Mark where leukocytes are.
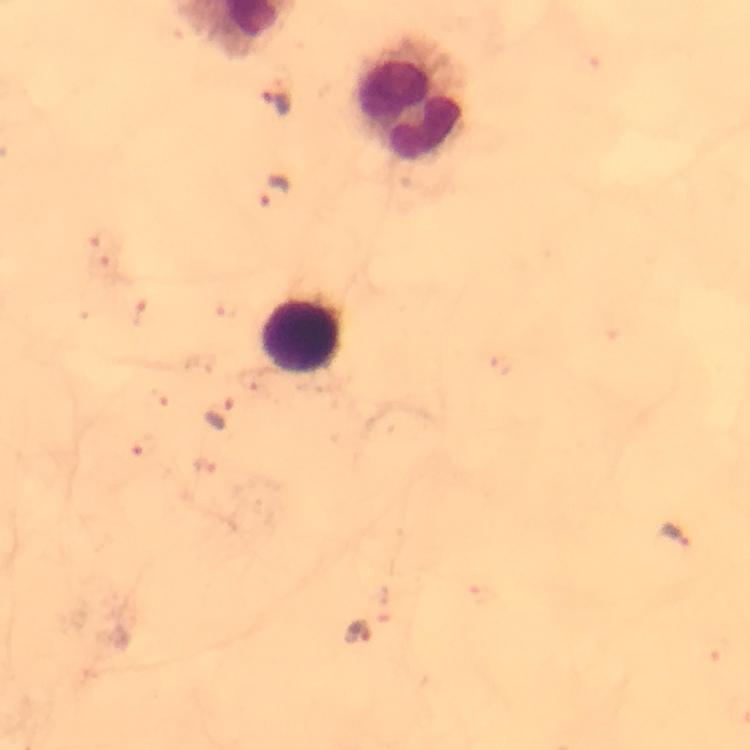
Approximate centers as [x, y] in pixels.
Leukocytes: [410, 98], [302, 337].

Summary:
  - Plasmodium parasite locations: [277, 101], [274, 190], [220, 416], [676, 536], [358, 633]
  - Immersion oil: used
  - Context: from a malaria diagnostic workup
  - Magnification: 100x
  - Stain: Giemsa
  - Capture: smartphone photograph through a microscope
  - Cropped from: a single field of view
  - Preparation: thick blood film
  - Image size: 750×750 pixels